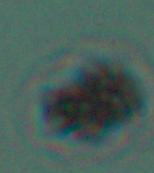
Summary:
  - Modality: micrograph
  - Identification: Leishmania
  - Magnification: 1000x